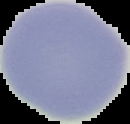 Cell region segmented out of the field of view; the surrounding area is masked to black. From a thin blood smear. Result: no malaria parasites seen. Image is 130×124 pixels.